Locate every uninfected red blood cell.
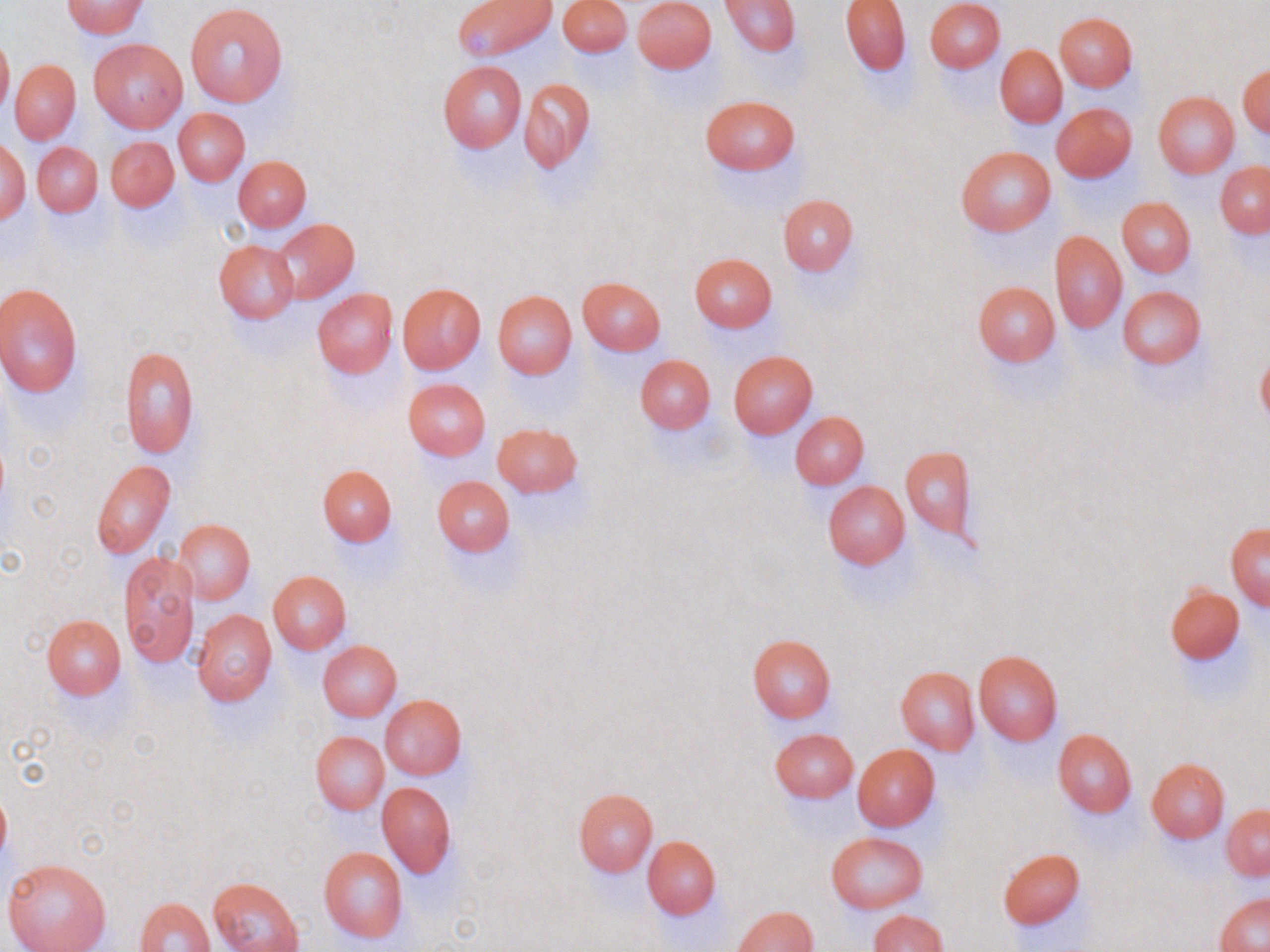
Approximate bounding boxes as [x1, y1, x2, y2] in pixels.
Uninfected red blood cells: [63, 0, 146, 37], [453, 0, 556, 60], [559, 0, 632, 55], [633, 0, 716, 72], [841, 0, 911, 75], [924, 0, 1004, 72], [721, 1, 799, 56], [185, 4, 290, 107], [1055, 13, 1137, 90], [0, 34, 13, 120], [88, 38, 187, 132], [995, 45, 1067, 127], [9, 59, 81, 143], [437, 59, 528, 153], [1239, 64, 1269, 136], [519, 78, 595, 171], [1153, 91, 1239, 178], [701, 95, 799, 175], [1052, 103, 1137, 181], [173, 108, 250, 185], [105, 136, 178, 211], [0, 138, 30, 225], [32, 142, 103, 217], [957, 145, 1056, 235], [235, 156, 311, 230], [1216, 161, 1270, 237], [778, 194, 857, 275], [1117, 197, 1195, 277], [274, 217, 360, 303], [1050, 230, 1127, 332], [213, 240, 299, 324], [689, 253, 778, 331], [577, 276, 666, 355], [972, 281, 1061, 366], [0, 283, 83, 397], [397, 283, 485, 374], [1118, 286, 1206, 369], [312, 288, 397, 377], [493, 290, 577, 378], [119, 345, 199, 459], [729, 350, 818, 437], [1256, 351, 1270, 428], [635, 354, 715, 433], [403, 379, 491, 460], [791, 411, 869, 488], [493, 423, 582, 497], [899, 445, 976, 546], [92, 460, 176, 558], [317, 464, 397, 546], [431, 475, 515, 556], [823, 481, 910, 568], [174, 518, 255, 604], [1226, 523, 1270, 610], [120, 552, 198, 669], [267, 570, 351, 654], [1164, 586, 1244, 662], [192, 610, 277, 705], [40, 614, 125, 699], [747, 633, 837, 724], [318, 641, 402, 721], [973, 649, 1064, 747], [895, 666, 980, 754], [380, 694, 466, 779], [771, 728, 857, 802], [1052, 728, 1137, 817], [311, 731, 389, 814], [852, 744, 940, 831], [1146, 758, 1229, 842], [378, 781, 457, 877], [573, 788, 658, 876], [0, 791, 11, 862], [1223, 804, 1269, 880], [826, 834, 927, 913], [641, 835, 721, 919], [318, 846, 409, 943], [998, 848, 1085, 930], [1, 857, 113, 952], [210, 877, 304, 952], [1215, 892, 1269, 952], [134, 896, 215, 952], [733, 905, 817, 951], [870, 910, 947, 952].

Slide-level diagnosis: negative for blood parasites. Image is 1270×952 pixels. 1000x magnification. Thin blood smear. Single field of view. Optical microscopy. May-Grünwald-Giemsa stain.